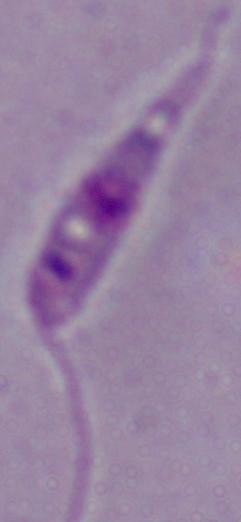 Micrograph. A Leishmania parasite is seen. Captured at 1000x magnification.